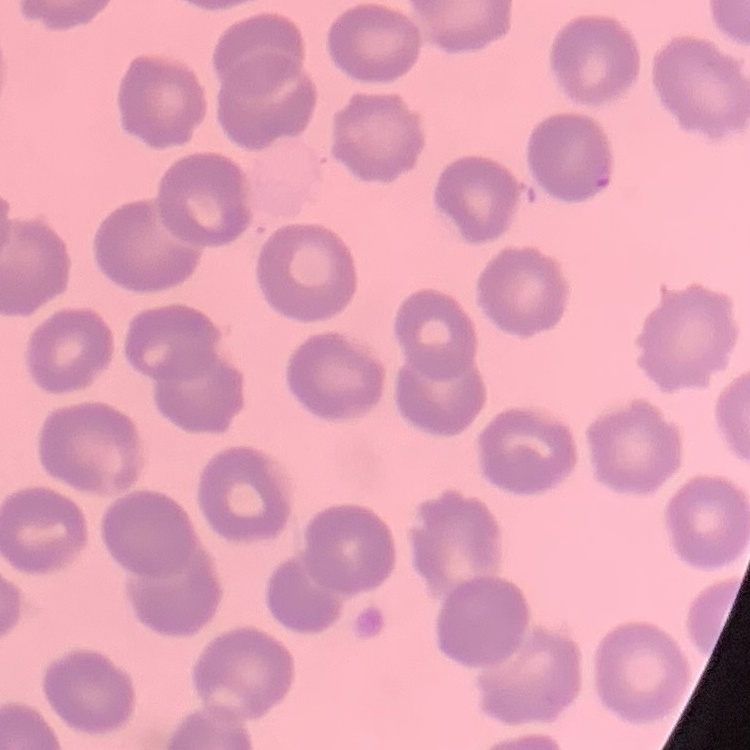 The red blood cells exhibit no rouleaux formation. Square crop of a larger photomicrograph. Stained with either Field's or Giemsa. Thin blood film.